Assess the morphology of the red blood cells.
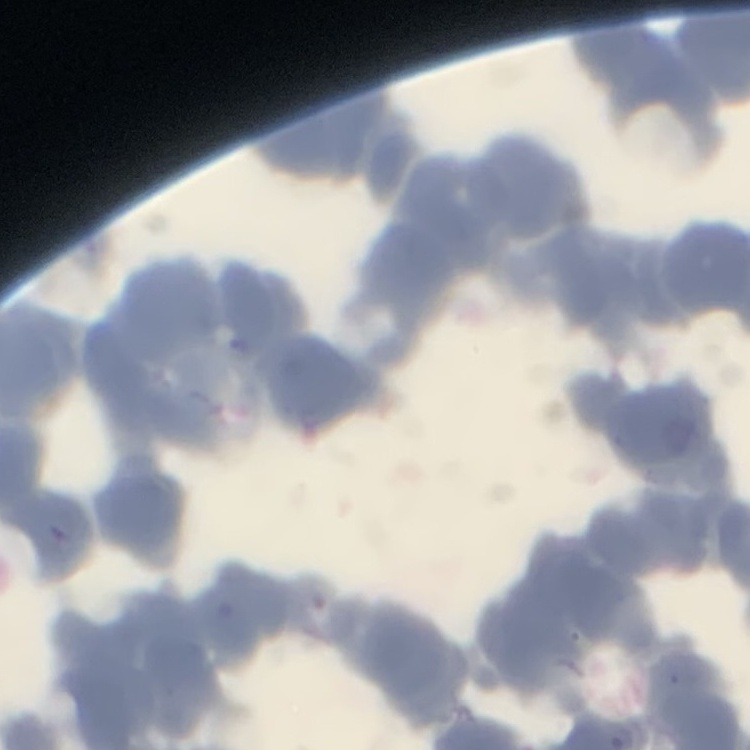
They show rouleaux formation.

Summary:
  - Preparation: thin blood smear
  - Image type: square crop of a larger photomicrograph
  - Stain: Field's or Giemsa